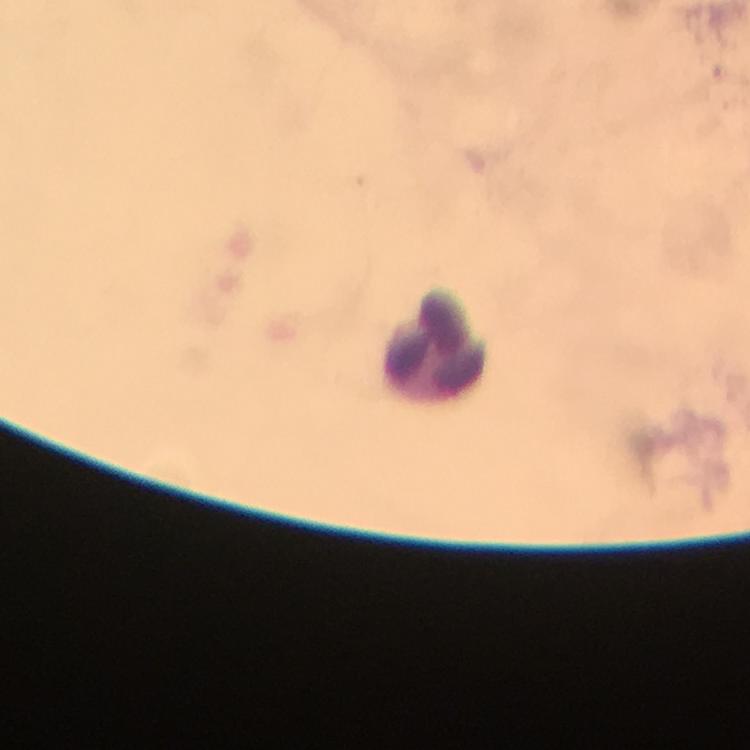
Approximate object centers, in pixels from the top-left corner. Leukocyte locations: (x=433, y=340). From a malaria diagnostic workup. Malaria parasites: none detected. Thick blood smear. A crop from one field of view. At 100x magnification. Immersion oil applied. Image is 750×750 pixels. Smartphone photograph taken through a microscope. Giemsa-stained preparation.